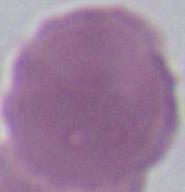

{
  "modality": "photomicrograph",
  "identification": "erythrocyte",
  "magnification": "1000x"
}